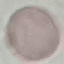
Summary:
  - Malaria status: uninfected
  - Preparation: thin blood film
  - Capture: smartphone camera at the microscope eyepiece
  - Image type: cell patch, automatically extracted from a larger field of view and resized to 64 × 64 pixels
  - Stain: Giemsa